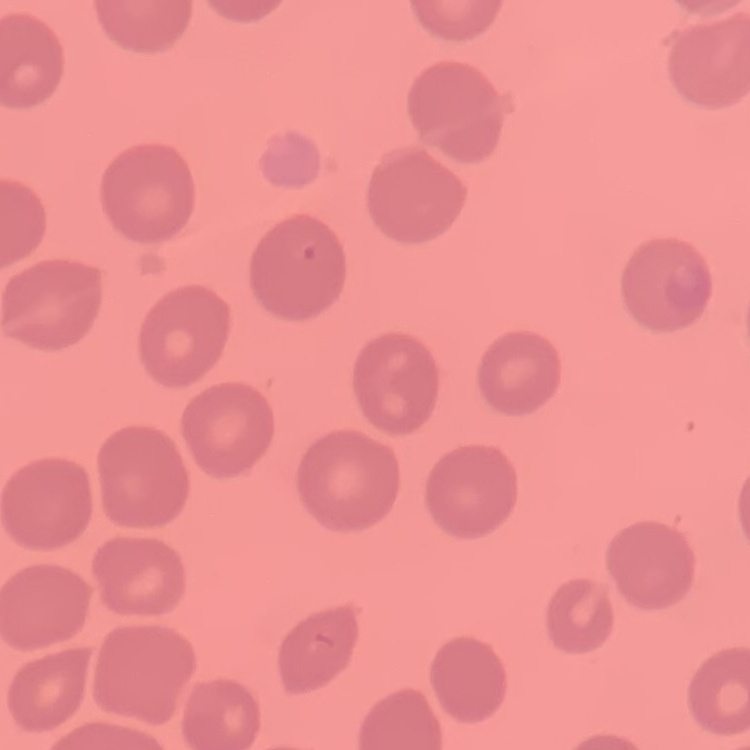

Summary:
  - Erythrocyte morphology: no rouleaux formation
  - Stain: Field's or Giemsa
  - Image type: square crop of a larger photomicrograph
  - Preparation: thin blood smear